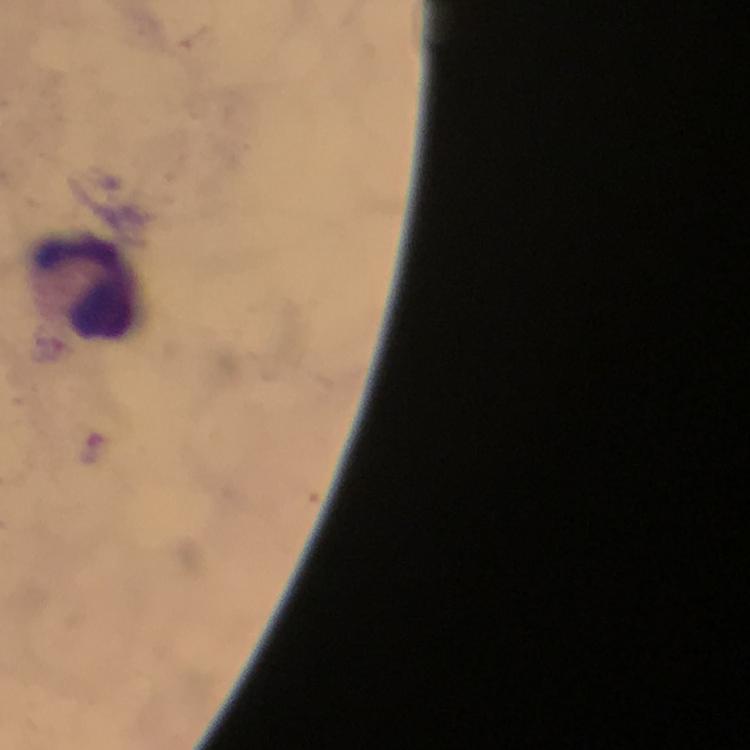 Approximate object centers, in pixels from the top-left corner. Leukocyte locations: (x=86, y=287). Plasmodium parasite locations: (x=92, y=449). Smartphone photograph taken through a microscope. From a malaria diagnostic workup. Immersion oil was used. Thick blood film. Giemsa stain. Image is 750×750 pixels. Cropped region of a single field of view. 100x magnification.